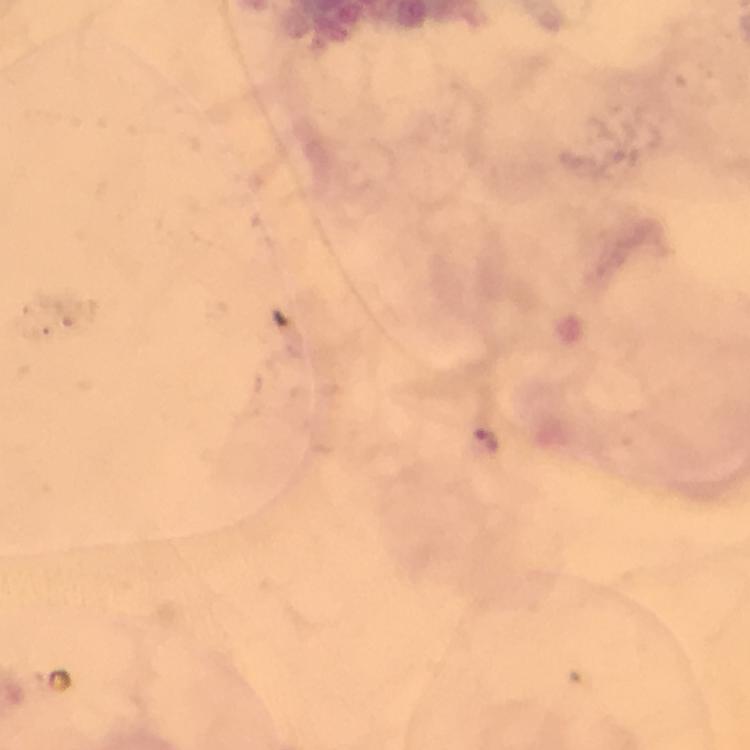
Approximate centers as [x, y] in pixels.
Summary:
  - Malaria parasite locations: [484, 440]
  - Stain: Giemsa
  - Capture: smartphone mounted on the microscope
  - Preparation: thick smear
  - Context: from a diagnostic examination for malaria
  - Image size: 750×750 pixels
  - Magnification: 100x
  - Immersion oil: used
  - Cropped from: one field of view